Name the blood parasite species.
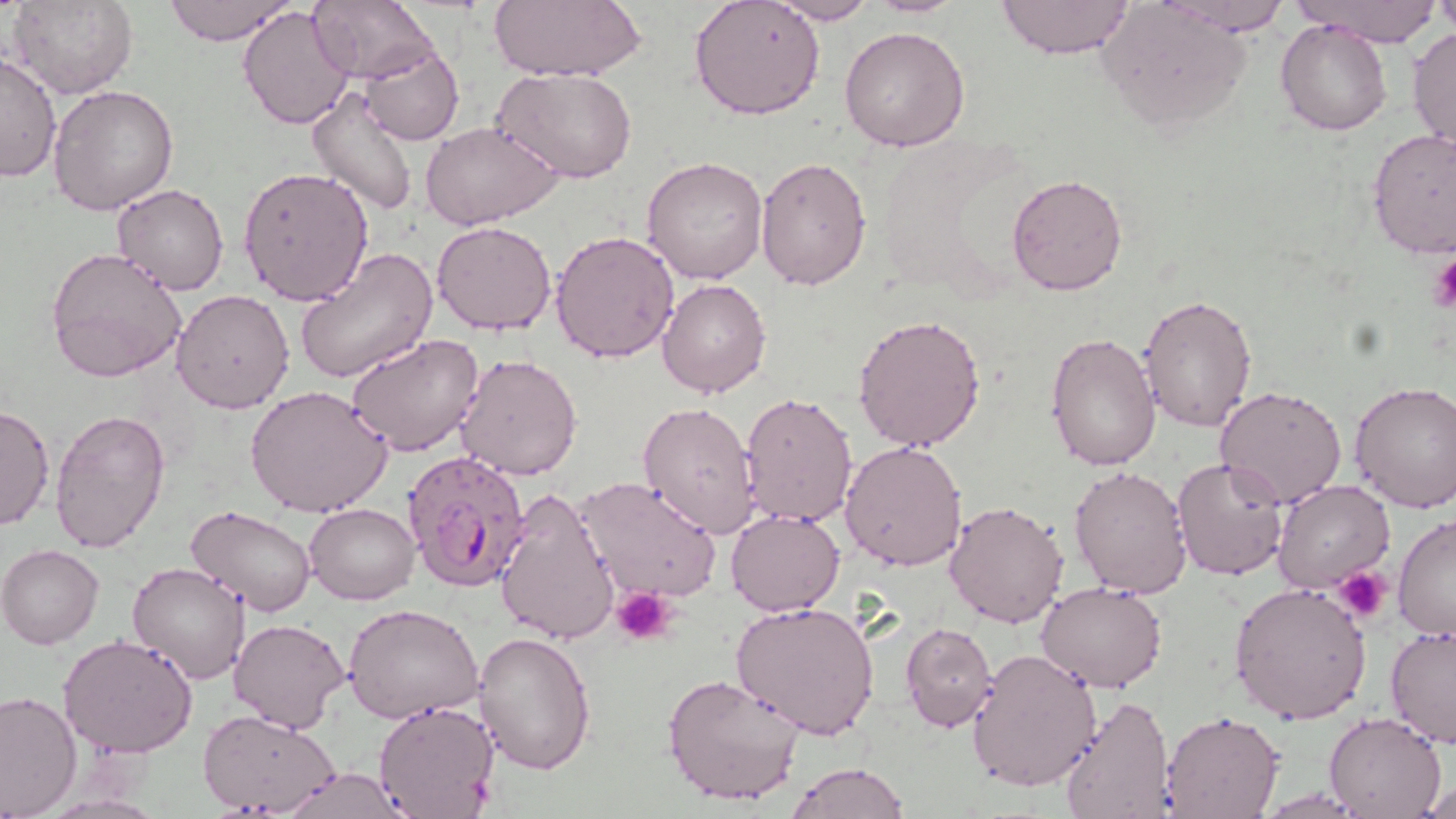
Plasmodium falciparum.

{
  "modality": "light microscopy",
  "plasmodium_falciparum_infected_red_blood_cell_locations": "approximate bounding boxes as named x1/y1/x2/y2 corners in pixels: (x1=402, y1=451, x2=534, y2=593)",
  "uninfected_red_blood_cell_locations": "approximate bounding boxes as named x1/y1/x2/y2 corners in pixels: (x1=10, y1=0, x2=137, y2=101), (x1=162, y1=0, x2=296, y2=45), (x1=309, y1=0, x2=440, y2=86), (x1=688, y1=0, x2=824, y2=121), (x1=996, y1=0, x2=1134, y2=60), (x1=1161, y1=0, x2=1291, y2=34), (x1=1293, y1=0, x2=1443, y2=47), (x1=486, y1=1, x2=647, y2=83), (x1=763, y1=1, x2=878, y2=25), (x1=1097, y1=1, x2=1252, y2=134), (x1=1431, y1=2, x2=1455, y2=35), (x1=237, y1=7, x2=356, y2=132), (x1=1276, y1=19, x2=1392, y2=136), (x1=839, y1=26, x2=971, y2=152), (x1=1408, y1=26, x2=1455, y2=156), (x1=359, y1=44, x2=464, y2=145), (x1=0, y1=51, x2=61, y2=183), (x1=495, y1=67, x2=637, y2=183), (x1=48, y1=84, x2=179, y2=215), (x1=307, y1=84, x2=419, y2=213), (x1=420, y1=120, x2=562, y2=230), (x1=1366, y1=129, x2=1456, y2=259), (x1=754, y1=155, x2=873, y2=290), (x1=642, y1=156, x2=768, y2=285), (x1=238, y1=165, x2=373, y2=306), (x1=1005, y1=172, x2=1129, y2=296), (x1=113, y1=183, x2=230, y2=295), (x1=431, y1=220, x2=558, y2=335), (x1=550, y1=229, x2=679, y2=363), (x1=46, y1=246, x2=188, y2=382), (x1=295, y1=247, x2=437, y2=384), (x1=656, y1=279, x2=771, y2=399), (x1=171, y1=288, x2=295, y2=413), (x1=1136, y1=294, x2=1257, y2=433), (x1=852, y1=312, x2=987, y2=453), (x1=1044, y1=330, x2=1161, y2=471), (x1=346, y1=334, x2=485, y2=458), (x1=455, y1=353, x2=583, y2=481), (x1=1349, y1=381, x2=1456, y2=512), (x1=245, y1=385, x2=393, y2=520), (x1=1214, y1=385, x2=1348, y2=509), (x1=737, y1=389, x2=857, y2=529), (x1=637, y1=403, x2=759, y2=536), (x1=0, y1=404, x2=54, y2=533), (x1=48, y1=407, x2=170, y2=555), (x1=840, y1=441, x2=968, y2=571), (x1=1172, y1=456, x2=1290, y2=581), (x1=1069, y1=464, x2=1194, y2=599), (x1=573, y1=476, x2=722, y2=602), (x1=1273, y1=479, x2=1395, y2=595), (x1=494, y1=488, x2=622, y2=646), (x1=943, y1=499, x2=1070, y2=629), (x1=304, y1=502, x2=418, y2=604), (x1=185, y1=505, x2=317, y2=618), (x1=726, y1=508, x2=847, y2=617), (x1=1393, y1=513, x2=1456, y2=641), (x1=1, y1=543, x2=104, y2=648), (x1=126, y1=562, x2=252, y2=685), (x1=1036, y1=580, x2=1167, y2=693), (x1=1228, y1=580, x2=1371, y2=724), (x1=732, y1=601, x2=880, y2=740), (x1=343, y1=604, x2=483, y2=724), (x1=228, y1=618, x2=349, y2=734), (x1=901, y1=621, x2=998, y2=733), (x1=1385, y1=622, x2=1456, y2=748), (x1=57, y1=633, x2=200, y2=758), (x1=473, y1=633, x2=596, y2=775), (x1=967, y1=648, x2=1102, y2=793), (x1=662, y1=672, x2=809, y2=810), (x1=0, y1=690, x2=82, y2=817), (x1=1056, y1=694, x2=1177, y2=818), (x1=372, y1=699, x2=500, y2=819), (x1=197, y1=708, x2=342, y2=817), (x1=1161, y1=712, x2=1284, y2=819), (x1=1323, y1=712, x2=1447, y2=818), (x1=787, y1=760, x2=910, y2=819), (x1=273, y1=766, x2=418, y2=819), (x1=1421, y1=781, x2=1453, y2=817)",
  "magnification": "1000x",
  "preparation": "thin blood film",
  "stain": "May-Grünwald-Giemsa",
  "image_size": "1456×819 pixels",
  "field_of_view": "one of a larger specimen",
  "platelet_locations": "approximate bounding boxes as named x1/y1/x2/y2 corners in pixels: (x1=1430, y1=254, x2=1456, y2=313), (x1=1334, y1=565, x2=1392, y2=624), (x1=613, y1=587, x2=675, y2=644)"
}